Locate and identify every blood parasite.
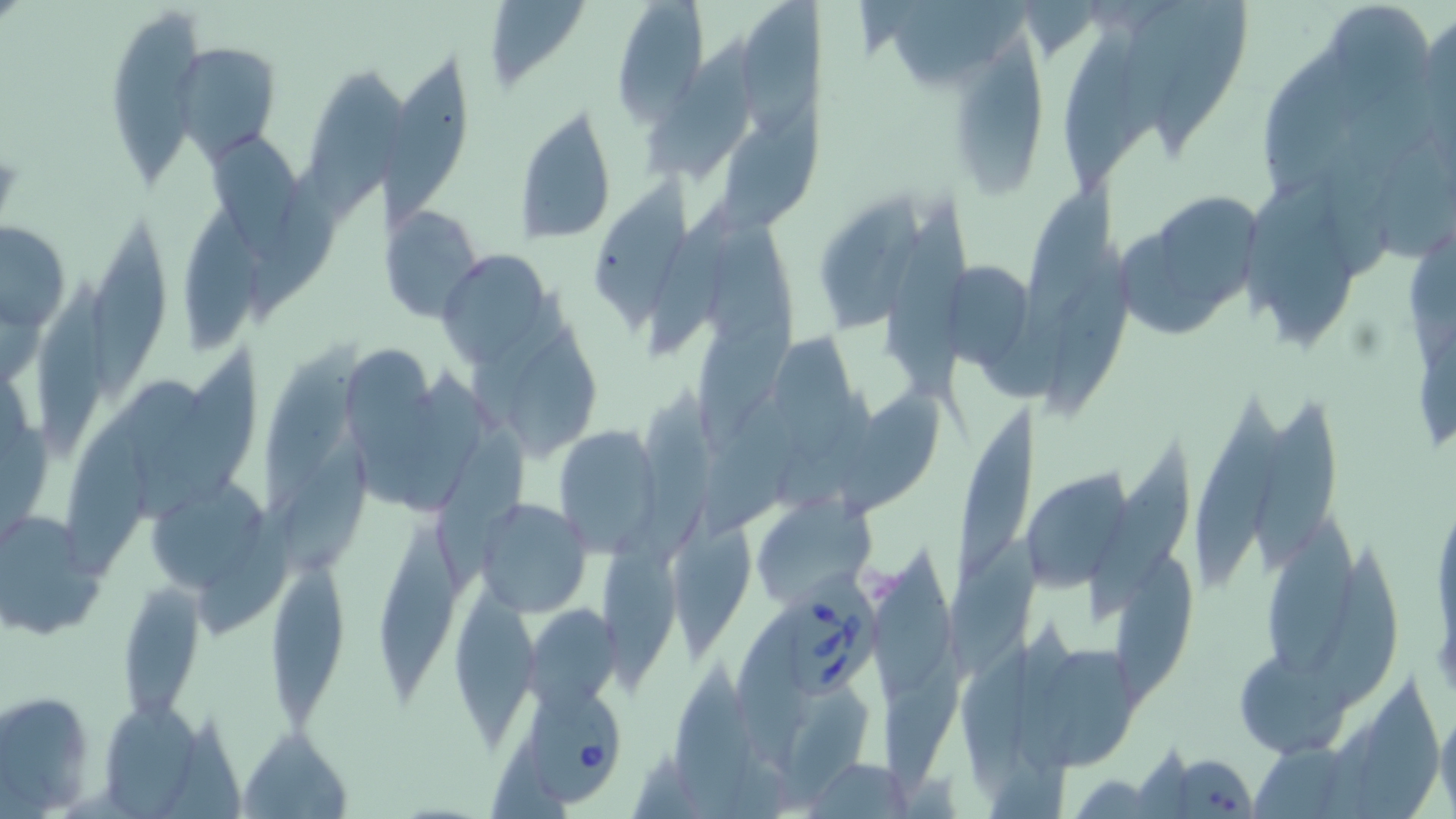
Approximate bounding boxes as [x1, y1, x2, y2] in pixels.
Babesia divergens-infected red blood cells: [784, 565, 879, 704], [519, 676, 629, 805].
No Plasmodium falciparum, Plasmodium ovale, Plasmodium malariae, Plasmodium vivax, or Trypanosoma brucei observed.

slide-level diagnosis = Babesia divergens
field of view = single
stain = May-Grünwald-Giemsa
magnification = 1000x
preparation = thin blood smear
uninfected red blood cell locations = approximate bounding boxes as [x1, y1, x2, y2] in pixels: [481, 0, 592, 94], [610, 0, 710, 121], [742, 0, 823, 140], [1319, 0, 1439, 103], [104, 6, 204, 190], [1418, 13, 1455, 144], [1062, 23, 1135, 196], [641, 27, 769, 182], [955, 40, 1045, 200], [174, 44, 279, 162], [1262, 54, 1364, 197], [381, 59, 470, 221], [307, 70, 402, 217], [713, 92, 827, 242], [513, 103, 617, 245], [208, 130, 304, 262], [1375, 142, 1456, 266], [248, 167, 339, 331], [591, 172, 693, 338], [1027, 178, 1118, 321], [1160, 194, 1260, 307], [823, 195, 921, 333], [184, 201, 264, 358], [648, 202, 735, 359], [877, 202, 976, 415], [379, 204, 483, 322], [88, 218, 171, 404], [1, 219, 70, 333], [1120, 231, 1220, 336], [1048, 248, 1137, 414], [438, 251, 549, 368], [945, 262, 1034, 369], [30, 272, 113, 463], [699, 306, 796, 456], [508, 328, 604, 466], [773, 329, 864, 465], [136, 341, 265, 526], [256, 341, 368, 512], [346, 348, 438, 469], [846, 381, 944, 516], [68, 382, 203, 578], [637, 388, 722, 562], [1249, 394, 1333, 568], [1188, 396, 1282, 595], [955, 401, 1041, 578], [698, 411, 809, 537], [553, 422, 662, 553], [436, 425, 527, 597], [280, 443, 374, 589], [1091, 443, 1194, 618], [1018, 468, 1133, 594], [144, 477, 271, 600], [749, 495, 875, 607], [476, 498, 592, 617], [0, 509, 109, 636], [672, 517, 755, 666], [1263, 518, 1355, 685], [595, 521, 685, 698], [376, 530, 462, 710], [949, 533, 1043, 682], [1309, 546, 1400, 710], [1116, 549, 1199, 706], [874, 553, 958, 702], [263, 564, 353, 728], [117, 579, 206, 722], [458, 592, 540, 743], [523, 604, 620, 712], [735, 612, 804, 778], [884, 644, 968, 799], [1019, 648, 1138, 772], [1237, 650, 1346, 757], [682, 665, 757, 811], [1353, 685, 1444, 819], [0, 690, 99, 812], [106, 696, 202, 818], [1436, 705, 1455, 814], [239, 726, 353, 817], [1150, 752, 1258, 818], [808, 758, 913, 816]
modality = light microscopy
image size = 1456×819 pixels